Assess this cell for malaria.
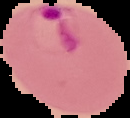

Parasitized.

Summary:
  - Image type: cell region segmented out of the field of view; surrounding area masked to black
  - Image size: 130×118 pixels
  - Preparation: thin blood smear